Classify this cell by malaria status.
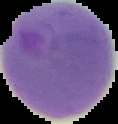

It is parasitized.

image type = segmented cell region with the area outside set to black
image size = 118×124 pixels
preparation = thin blood smear